Locate every Plasmodium parasite.
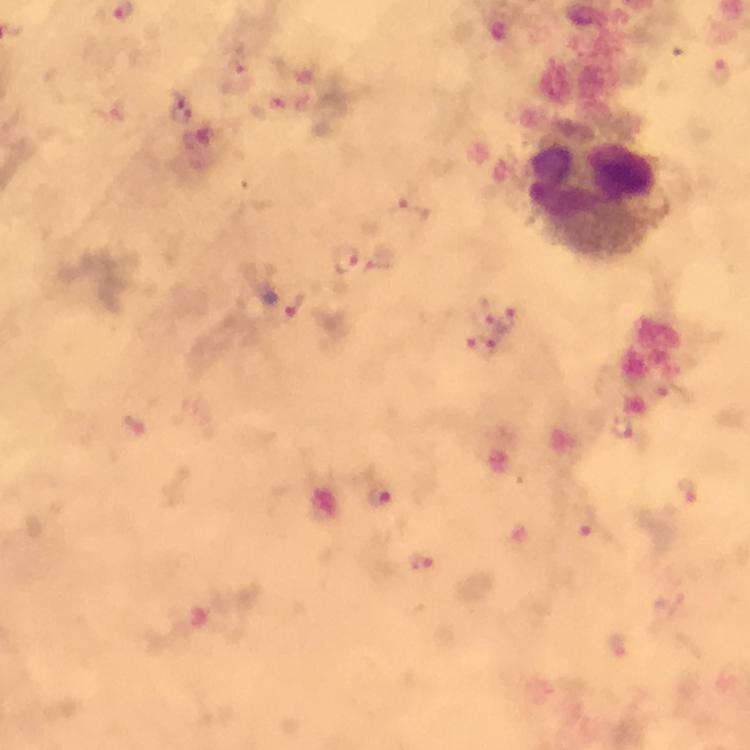

Approximate centers as {x, y} in pixels.
Plasmodium parasites: {719, 73}, {181, 109}, {409, 211}, {346, 261}, {502, 316}, {482, 343}, {623, 427}, {381, 493}, {688, 494}, {585, 522}, {420, 561}.

Summary:
  - Leukocyte locations: {597, 200}
  - Context: from a malaria diagnostic workup
  - Preparation: thick blood film
  - Cropped from: one field of view
  - Stain: Giemsa
  - Image size: 750×750 pixels
  - Immersion oil: applied
  - Capture: smartphone mounted on the microscope
  - Magnification: 100x